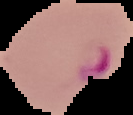

Summary:
  - Image size: 133×115 pixels
  - Preparation: thin blood smear
  - Result: malaria parasites detected
  - Image type: segmented cell region with the area outside set to black